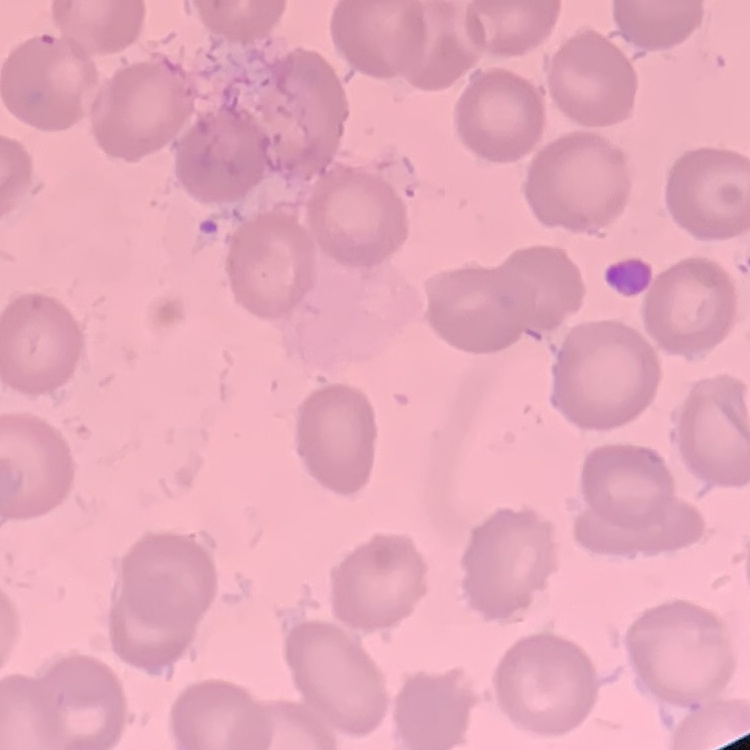
{
  "red_blood_cell_morphology": "no rouleaux formation",
  "stain": "Field's or Giemsa",
  "preparation": "thin blood smear",
  "image_type": "one tile cut from a larger photomicrograph"
}